Identify the blood parasite species.
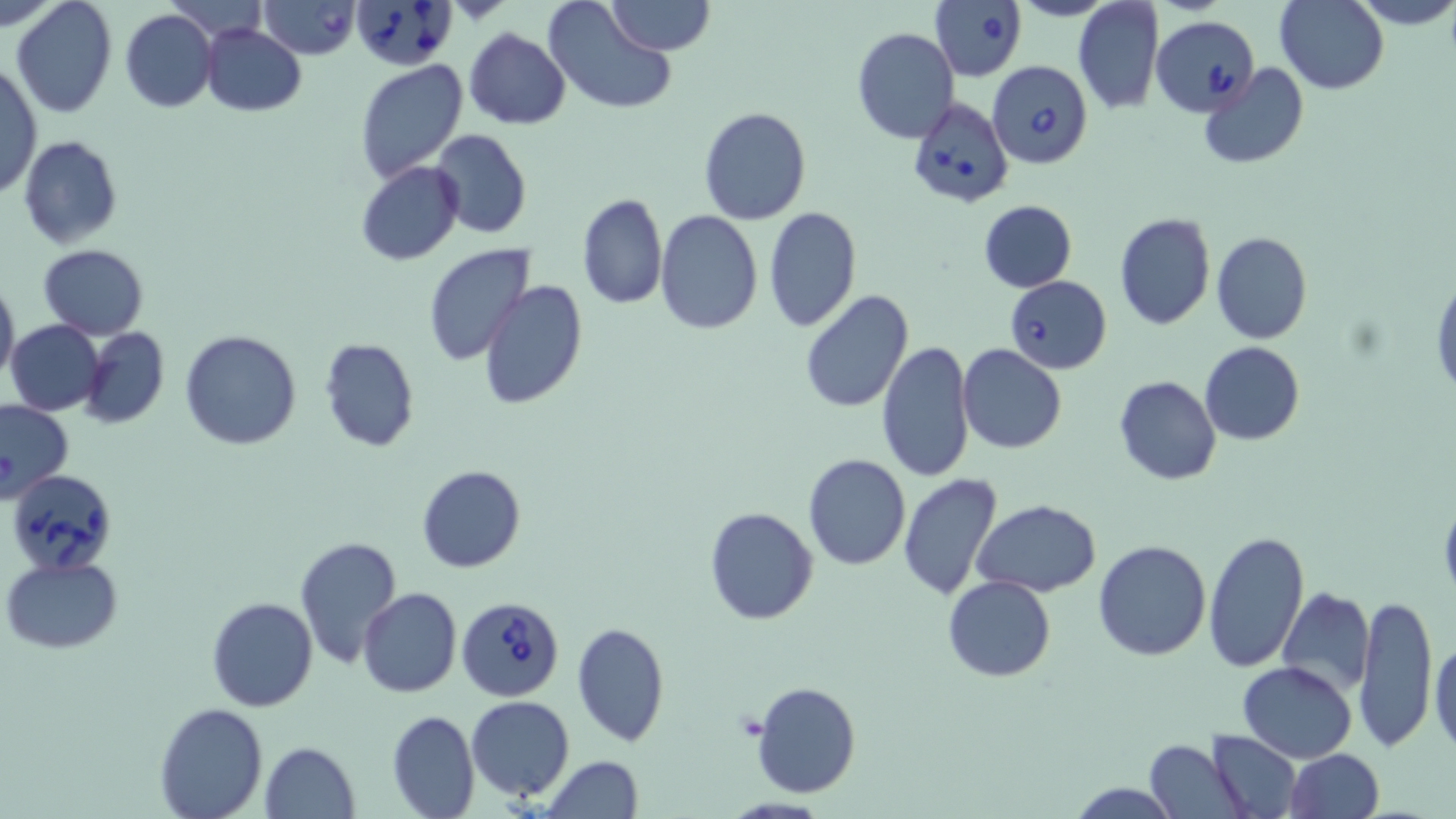
Babesia divergens.

field of view = one of a larger specimen
preparation = thin blood film
modality = light microscopy
platelet locations = approximate bounding boxes as (x1,y1)-(x2,y2) corner pairs in pixels: (734,711)-(768,740)
uninfected red blood cell locations = approximate bounding boxes as (x1,y1)-(x2,y2) corner pairs in pixels: (2,0)-(64,31), (11,0)-(118,118), (608,0)-(713,56), (1073,0)-(1165,116), (1349,0)-(1456,30), (542,1)-(679,117), (1274,1)-(1388,93), (120,9)-(217,112), (201,24)-(307,115), (852,28)-(960,145), (464,29)-(571,129), (1,61)-(41,203), (355,61)-(468,183), (1199,63)-(1310,169), (698,106)-(811,225), (430,129)-(532,239), (19,136)-(122,249), (357,162)-(464,265), (576,193)-(668,309), (978,198)-(1077,292), (764,208)-(860,331), (656,210)-(763,334), (1115,212)-(1215,329), (1210,231)-(1312,345), (38,244)-(149,339), (423,244)-(533,365), (1431,274)-(1455,404), (0,278)-(19,387), (479,281)-(588,410), (799,289)-(914,414), (7,320)-(106,417), (78,326)-(169,429), (180,330)-(301,450), (318,338)-(419,453), (877,339)-(974,482), (1200,341)-(1305,445), (958,343)-(1066,454), (1114,376)-(1221,485), (0,399)-(74,501), (803,453)-(912,571), (416,465)-(525,572), (898,473)-(1004,600), (1438,495)-(1456,602), (973,499)-(1101,597), (703,506)-(818,625), (1203,528)-(1311,673), (295,535)-(405,670), (1092,538)-(1213,661), (2,555)-(122,654), (942,575)-(1055,681), (1275,586)-(1374,697), (358,588)-(462,698), (1355,591)-(1438,751), (207,596)-(318,712), (571,621)-(671,747), (1430,637)-(1456,757), (1237,661)-(1358,761), (752,681)-(861,800), (466,695)-(574,800), (155,702)-(269,819), (386,709)-(479,819), (1208,730)-(1302,817), (1143,740)-(1245,817), (260,741)-(361,819), (1283,749)-(1384,819), (541,757)-(644,818), (1069,783)-(1169,818)
magnification = 1000x
image size = 1456×819 pixels
stain = May-Grünwald-Giemsa
Babesia divergens-infected red blood cell locations = approximate bounding boxes as (x1,y1)-(x2,y2) corner pairs in pixels: (259,0)-(360,59), (351,0)-(457,70), (929,0)-(1028,82), (1150,16)-(1258,115), (989,60)-(1094,170), (907,97)-(1014,209), (1004,276)-(1112,374), (7,469)-(117,571), (456,596)-(565,701)